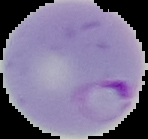
From a thin blood film. Image is 148×139 pixels. The area outside the segmented cell region is set to black. Malaria status: parasitized.